Outline each Plasmodium ovale-infected red blood cell.
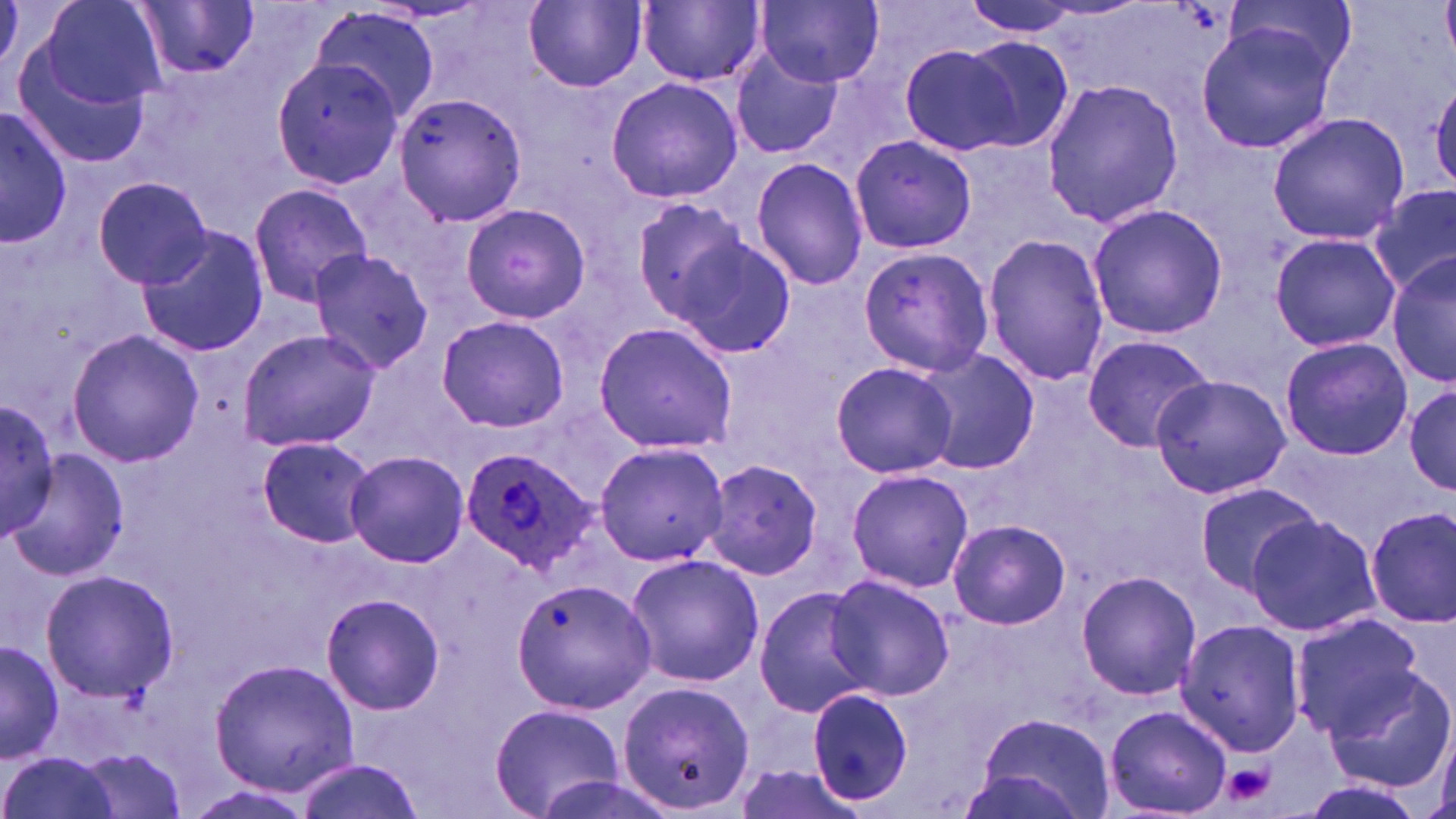

Approximate bounding boxes as named x1/y1/x2/y2 corners in pixels.
Plasmodium ovale-infected red blood cells: (x1=458, y1=444, x2=598, y2=576).

Summary:
  - Uninfected red blood cell locations: (x1=41, y1=0, x2=167, y2=110), (x1=756, y1=0, x2=885, y2=88), (x1=963, y1=0, x2=1091, y2=36), (x1=1219, y1=0, x2=1358, y2=99), (x1=523, y1=1, x2=647, y2=92), (x1=639, y1=1, x2=765, y2=87), (x1=133, y1=2, x2=261, y2=80), (x1=311, y1=5, x2=441, y2=123), (x1=1195, y1=19, x2=1340, y2=154), (x1=959, y1=36, x2=1077, y2=154), (x1=14, y1=41, x2=155, y2=168), (x1=898, y1=41, x2=1029, y2=158), (x1=729, y1=44, x2=842, y2=160), (x1=270, y1=57, x2=406, y2=188), (x1=1426, y1=73, x2=1456, y2=194), (x1=605, y1=76, x2=743, y2=205), (x1=1040, y1=79, x2=1185, y2=226), (x1=393, y1=91, x2=528, y2=229), (x1=1, y1=105, x2=72, y2=249), (x1=1266, y1=111, x2=1412, y2=246), (x1=850, y1=133, x2=979, y2=254), (x1=750, y1=157, x2=870, y2=289), (x1=93, y1=177, x2=215, y2=288), (x1=248, y1=183, x2=374, y2=307), (x1=1372, y1=185, x2=1456, y2=296), (x1=629, y1=195, x2=753, y2=333), (x1=460, y1=203, x2=591, y2=324), (x1=1086, y1=203, x2=1227, y2=341), (x1=134, y1=225, x2=270, y2=358), (x1=1267, y1=231, x2=1399, y2=353), (x1=671, y1=233, x2=799, y2=360), (x1=980, y1=233, x2=1110, y2=388), (x1=856, y1=245, x2=993, y2=377), (x1=307, y1=246, x2=437, y2=373), (x1=1386, y1=250, x2=1456, y2=391), (x1=435, y1=315, x2=570, y2=431), (x1=591, y1=319, x2=738, y2=455), (x1=65, y1=328, x2=204, y2=467), (x1=237, y1=329, x2=380, y2=453), (x1=1081, y1=334, x2=1215, y2=452), (x1=1279, y1=336, x2=1413, y2=461), (x1=910, y1=348, x2=1040, y2=477), (x1=828, y1=359, x2=961, y2=480), (x1=1149, y1=374, x2=1292, y2=499), (x1=1405, y1=381, x2=1456, y2=499), (x1=0, y1=397, x2=60, y2=546), (x1=255, y1=435, x2=374, y2=548), (x1=590, y1=441, x2=732, y2=568), (x1=345, y1=450, x2=469, y2=568), (x1=13, y1=455, x2=128, y2=579), (x1=700, y1=457, x2=825, y2=582), (x1=846, y1=466, x2=974, y2=593), (x1=1193, y1=480, x2=1323, y2=595), (x1=1365, y1=506, x2=1454, y2=631), (x1=1246, y1=514, x2=1382, y2=637), (x1=947, y1=519, x2=1070, y2=631), (x1=624, y1=554, x2=765, y2=687), (x1=41, y1=568, x2=180, y2=702), (x1=1075, y1=570, x2=1202, y2=701), (x1=510, y1=574, x2=660, y2=713), (x1=826, y1=574, x2=956, y2=701), (x1=753, y1=585, x2=879, y2=719), (x1=320, y1=592, x2=447, y2=716), (x1=1288, y1=613, x2=1429, y2=740), (x1=1176, y1=618, x2=1309, y2=758), (x1=0, y1=639, x2=62, y2=764), (x1=209, y1=657, x2=360, y2=796), (x1=1322, y1=664, x2=1456, y2=793), (x1=619, y1=679, x2=754, y2=814), (x1=805, y1=687, x2=914, y2=807), (x1=489, y1=704, x2=624, y2=817), (x1=1105, y1=705, x2=1230, y2=816), (x1=974, y1=713, x2=1116, y2=819), (x1=75, y1=748, x2=189, y2=819), (x1=1, y1=752, x2=119, y2=819), (x1=292, y1=755, x2=426, y2=819)
  - Platelet locations: (x1=1223, y1=762, x2=1275, y2=805)
  - Slide-level diagnosis: Plasmodium ovale
  - Modality: optical microscopy
  - Preparation: thin blood smear
  - Field of view: single
  - Stain: May-Grünwald-Giemsa
  - Image size: 1456×819 pixels
  - Magnification: 1000x